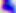
Micrograph. 400x magnification. Toxoplasma gondii is shown.